Locate the cells, classifying each as a parasitized red blood cell, an uninfected red blood cell, or a white blood cell.
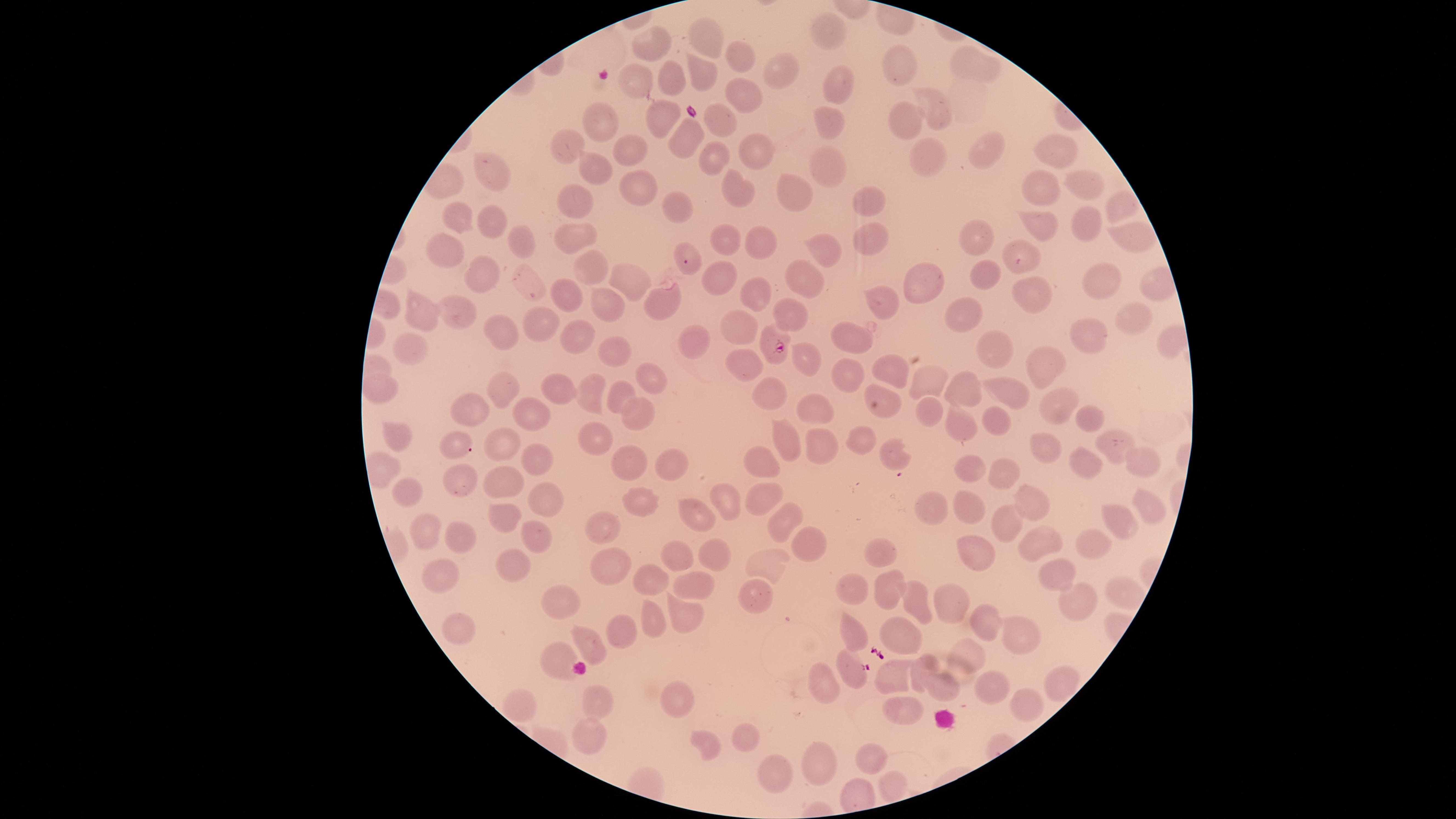
Approximate marker points as (x, y) in pixels.
Parasitized red blood cells: (777, 347), (852, 670).
Uninfected red blood cells: (824, 31), (707, 40), (652, 48), (736, 59), (972, 61), (899, 62), (780, 71), (702, 77), (673, 78), (637, 79), (837, 82), (743, 96), (940, 111), (657, 114), (909, 117), (602, 120), (719, 121), (830, 121), (683, 141), (574, 145), (625, 149), (987, 149), (755, 151), (1058, 154), (931, 157), (716, 159), (831, 164), (594, 168), (497, 174), (1039, 186), (640, 187), (1078, 189), (799, 192), (740, 193), (869, 199), (577, 200), (1116, 204), (676, 209), (458, 220), (492, 221), (1045, 225), (1089, 225), (575, 232), (1126, 235), (873, 236), (973, 237), (517, 240), (726, 240), (760, 244), (825, 246), (447, 248), (1024, 252), (589, 268), (978, 276), (722, 277), (486, 278), (804, 278), (1099, 278), (918, 280), (621, 281), (531, 282), (1033, 291), (566, 292), (761, 293), (886, 294), (662, 299), (607, 304), (796, 312), (457, 315), (424, 316), (540, 317), (1134, 320), (960, 327), (742, 330), (500, 333), (577, 335), (859, 337), (1090, 337), (692, 343), (413, 347), (994, 349), (615, 351), (807, 356), (895, 362), (750, 364), (1046, 364), (849, 374), (927, 377), (653, 380), (590, 385), (1011, 385), (773, 387), (964, 387), (382, 389), (563, 392), (622, 394), (501, 395), (880, 395), (1056, 403), (924, 406), (815, 410), (472, 414), (1085, 416), (534, 417), (992, 418), (637, 425), (393, 427), (597, 432), (960, 432), (788, 440), (857, 440), (1046, 440), (1109, 441), (456, 443), (505, 444), (818, 444), (897, 451), (672, 459), (531, 460), (1091, 460), (1140, 460), (633, 464), (763, 464), (968, 474), (1002, 478), (498, 482), (464, 486), (764, 490), (406, 493), (732, 495), (538, 497), (1028, 500), (634, 502), (939, 505), (967, 506), (1146, 510), (504, 517), (698, 518), (1118, 518), (783, 519), (1006, 525), (607, 527), (424, 528), (531, 534), (1044, 536), (460, 539), (1094, 539), (803, 546), (875, 548), (712, 552), (974, 553), (678, 559), (608, 562), (514, 564), (766, 568), (448, 573), (1063, 573), (656, 580), (892, 589), (693, 590), (854, 594), (753, 597), (921, 598), (955, 600), (1077, 600), (565, 602), (687, 617), (651, 619), (462, 620), (984, 622), (901, 630), (626, 633), (1019, 635), (856, 636), (589, 643), (966, 655), (562, 662), (921, 668), (895, 672), (823, 680), (1057, 683), (944, 685), (988, 686), (684, 695), (1021, 704), (597, 706), (901, 707), (740, 736), (588, 737), (709, 741), (877, 752), (820, 761), (774, 769), (888, 788).
No white blood cells identified.

{
  "field_of_view": "single",
  "stain": "Giemsa",
  "species": "Plasmodium falciparum",
  "image_size": "1456×819 pixels",
  "preparation": "thin blood smear",
  "visible_region": "circular",
  "capture": "smartphone photograph through the microscope eyepiece"
}